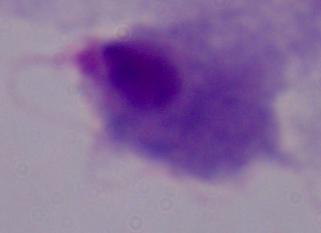

modality = photomicrograph
magnification = 1000x
identification = trichomonad